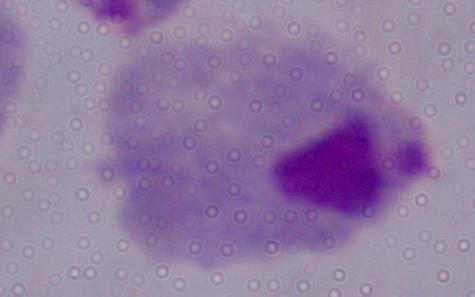

A trichomonad is seen. Photomicrograph. 1000x magnification.